Classify this cell by malaria status.
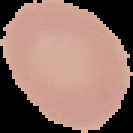
Uninfected.

preparation = thin blood film
image size = 133×133 pixels
image type = cell region segmented out of the field of view; surrounding area masked to black